Identify the parasite.
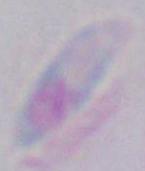

Toxoplasma gondii.

Micrograph. 1000x magnification.